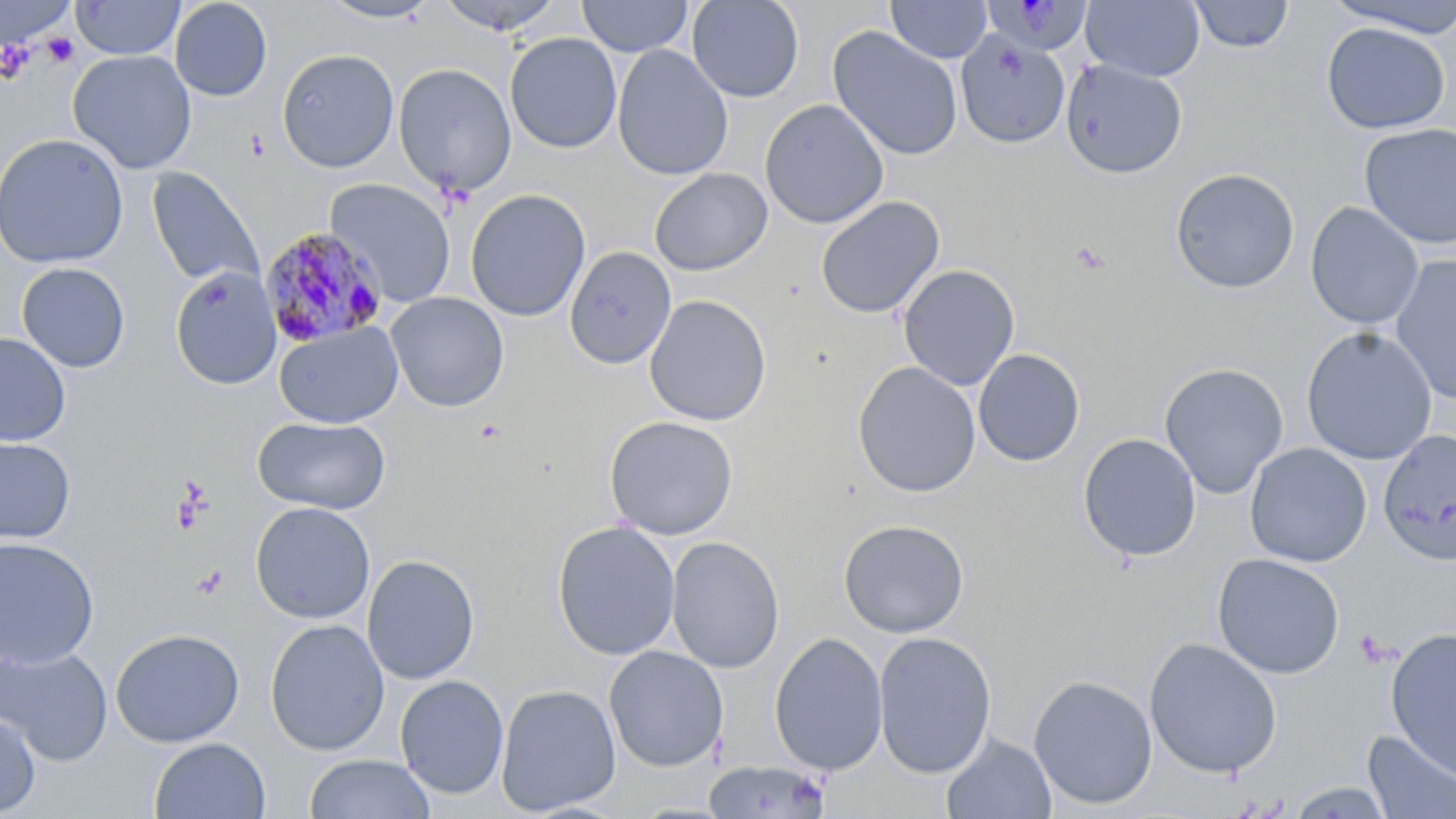
Summary:
  - Coordinate format: approximate bounding boxes as (x1, y1, x2, y2) in pixels
  - Uninfected red blood cell locations: (169, 0, 273, 102), (316, 0, 442, 25), (436, 0, 566, 35), (577, 0, 694, 57), (686, 0, 804, 102), (1081, 0, 1205, 82), (1323, 0, 1456, 37), (71, 1, 185, 60), (887, 1, 992, 64), (1188, 1, 1294, 54), (1320, 22, 1451, 135), (827, 26, 964, 162), (504, 32, 622, 154), (954, 32, 1070, 149), (611, 45, 733, 181), (277, 48, 399, 173), (67, 50, 197, 175), (1061, 60, 1187, 179), (393, 63, 516, 197), (759, 99, 889, 229), (1358, 123, 1456, 250), (0, 133, 128, 269), (147, 167, 265, 291), (649, 167, 773, 277), (1169, 168, 1300, 294), (325, 178, 456, 307), (465, 188, 591, 322), (815, 196, 945, 319), (1305, 202, 1424, 330), (564, 246, 676, 370), (1391, 255, 1456, 405), (16, 262, 131, 373), (897, 264, 1020, 390), (169, 265, 282, 391), (386, 292, 510, 412), (644, 295, 772, 426), (274, 321, 403, 428), (1300, 326, 1437, 465), (0, 332, 71, 446), (973, 348, 1085, 466), (852, 361, 981, 498), (1159, 362, 1289, 499), (252, 415, 391, 514), (603, 415, 739, 540), (1378, 429, 1456, 566), (1078, 433, 1201, 563), (0, 436, 77, 545), (1245, 442, 1372, 567), (249, 501, 376, 624), (838, 518, 969, 639), (552, 521, 680, 660), (0, 536, 100, 669), (666, 536, 785, 673), (1211, 553, 1346, 679), (361, 554, 480, 685), (265, 619, 390, 756), (110, 627, 245, 748), (1385, 627, 1456, 779), (873, 630, 997, 778), (769, 632, 888, 776), (1144, 637, 1282, 779), (1, 644, 113, 765), (604, 645, 729, 772), (394, 674, 509, 799), (1028, 675, 1157, 810), (495, 683, 621, 816), (0, 707, 41, 818), (1362, 730, 1456, 818), (941, 734, 1056, 818), (149, 737, 271, 819), (303, 754, 435, 819), (701, 759, 832, 819), (1284, 782, 1397, 818)
  - Platelet locations: (27, 15, 80, 62), (41, 32, 79, 68), (0, 39, 36, 86), (246, 128, 270, 160), (1355, 630, 1392, 667)
  - Plasmodium malariae-infected red blood cell locations: (984, 0, 1094, 57), (260, 227, 388, 348)
  - Slide-level diagnosis: Plasmodium malariae
  - Modality: optical microscopy
  - Preparation: thin blood smear
  - Field of view: single
  - Magnification: 1000x
  - Stain: May-Grünwald-Giemsa
  - Image size: 1456×819 pixels